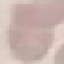

malaria status = uninfected
image type = cell patch, automatically extracted from a larger field of view and resized to 64 × 64 pixels
stain = Giemsa
preparation = thin smear
capture = smartphone through the microscope eyepiece